State the blood parasite species.
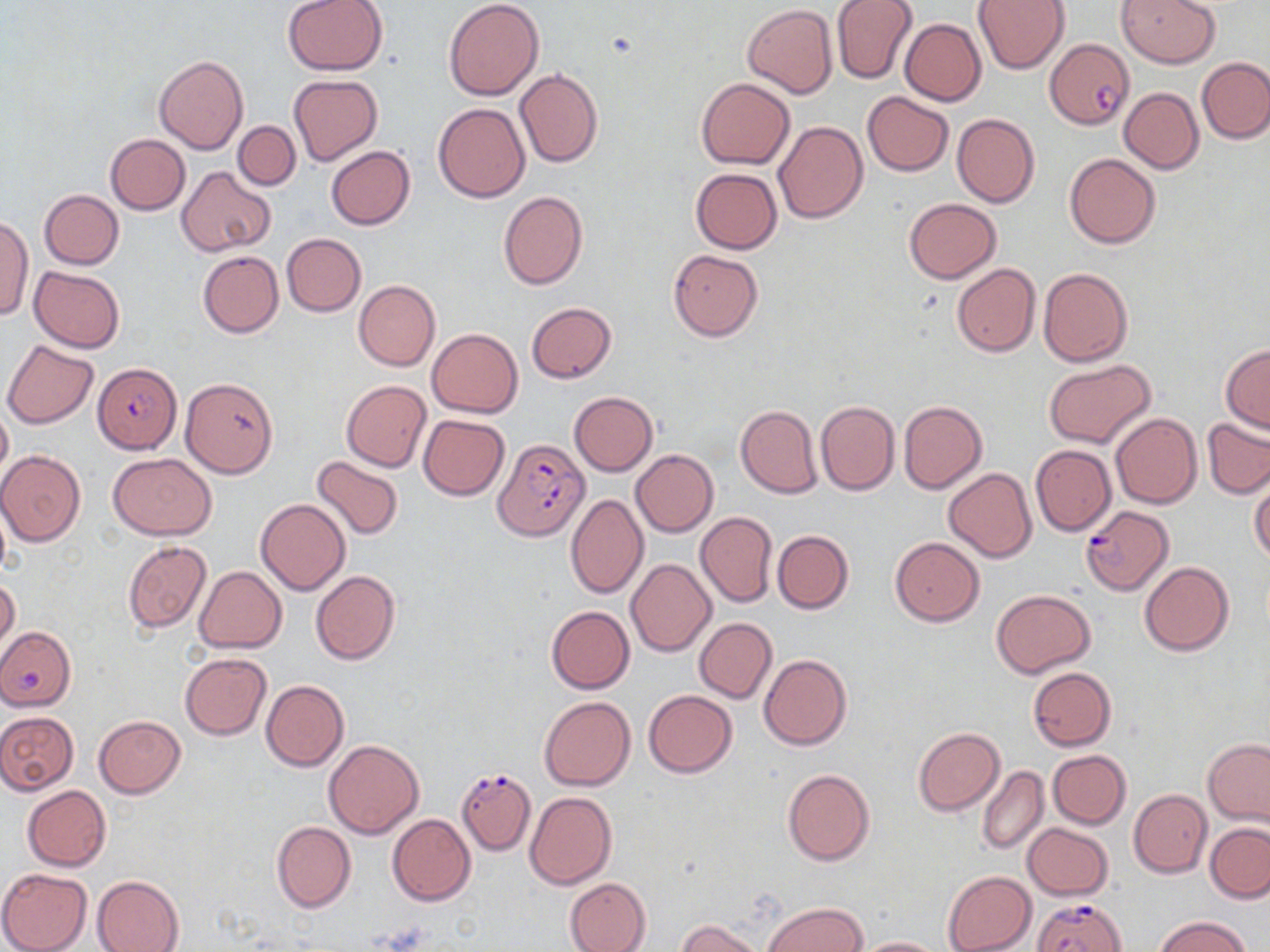
Plasmodium falciparum.

field of view = single
Plasmodium falciparum-infected red blood cell locations = approximate bounding boxes as (x1, y1, x2, y2) in pixels: (1044, 40, 1134, 129), (94, 363, 181, 454), (493, 438, 590, 541), (1081, 505, 1172, 594), (456, 767, 537, 854), (1032, 896, 1127, 952)
image size = 1270×952 pixels
uninfected red blood cell locations = approximate bounding boxes as (x1, y1, x2, y2) in pixels: (282, 0, 390, 75), (443, 0, 543, 100), (1117, 0, 1221, 68), (831, 1, 918, 84), (974, 1, 1070, 73), (742, 5, 838, 99), (899, 18, 985, 106), (154, 55, 247, 154), (1197, 57, 1270, 143), (515, 70, 604, 168), (289, 74, 383, 168), (695, 77, 795, 169), (1119, 88, 1203, 174), (862, 91, 954, 176), (433, 102, 530, 202), (952, 113, 1040, 209), (774, 120, 868, 223), (232, 121, 300, 190), (104, 133, 190, 214), (326, 146, 415, 230), (1065, 153, 1160, 248), (178, 166, 275, 256), (691, 168, 782, 254), (39, 189, 123, 269), (498, 191, 587, 289), (904, 198, 999, 282), (0, 215, 32, 319), (282, 233, 366, 316), (668, 249, 763, 341), (197, 251, 284, 338), (951, 263, 1040, 357), (29, 267, 124, 353), (1038, 267, 1133, 367), (353, 279, 440, 372), (526, 303, 617, 384), (426, 328, 523, 417), (2, 339, 98, 429), (1221, 344, 1270, 432), (1043, 359, 1156, 449), (179, 377, 278, 478), (341, 379, 431, 471), (569, 391, 658, 476), (816, 399, 899, 496), (899, 400, 987, 495), (0, 404, 12, 485), (735, 404, 823, 498), (1109, 413, 1201, 509), (418, 414, 509, 501), (1202, 418, 1270, 500), (1030, 444, 1117, 536), (631, 449, 718, 536), (1, 450, 87, 546), (108, 452, 216, 540), (311, 455, 404, 540), (944, 467, 1036, 562), (1249, 477, 1270, 566), (565, 494, 649, 599), (256, 498, 351, 595), (695, 513, 778, 607), (773, 530, 854, 614), (890, 537, 985, 626), (122, 541, 211, 634), (626, 558, 716, 656), (1140, 561, 1234, 656), (195, 565, 287, 653), (310, 570, 400, 665), (0, 577, 20, 652), (991, 589, 1095, 677), (546, 606, 634, 693), (694, 618, 777, 703), (0, 623, 75, 712), (180, 653, 271, 739), (758, 653, 852, 751), (1028, 668, 1115, 750), (261, 680, 349, 772), (644, 690, 738, 777), (539, 696, 636, 791), (0, 711, 78, 794), (92, 715, 185, 798), (913, 727, 1004, 815), (1203, 738, 1270, 826), (324, 739, 424, 839), (1048, 750, 1131, 829), (977, 765, 1048, 855), (782, 769, 875, 866), (22, 786, 111, 872), (1129, 789, 1212, 878), (525, 791, 616, 889), (388, 814, 476, 906), (271, 821, 355, 913), (1023, 823, 1113, 900), (1205, 823, 1270, 903), (0, 868, 92, 952), (942, 870, 1037, 952), (92, 874, 184, 952), (564, 876, 651, 952), (764, 902, 867, 952), (1154, 915, 1252, 952), (676, 918, 762, 952), (855, 936, 944, 952)
magnification = 1000x
modality = light microscopy
preparation = thin blood film
stain = May-Grünwald-Giemsa